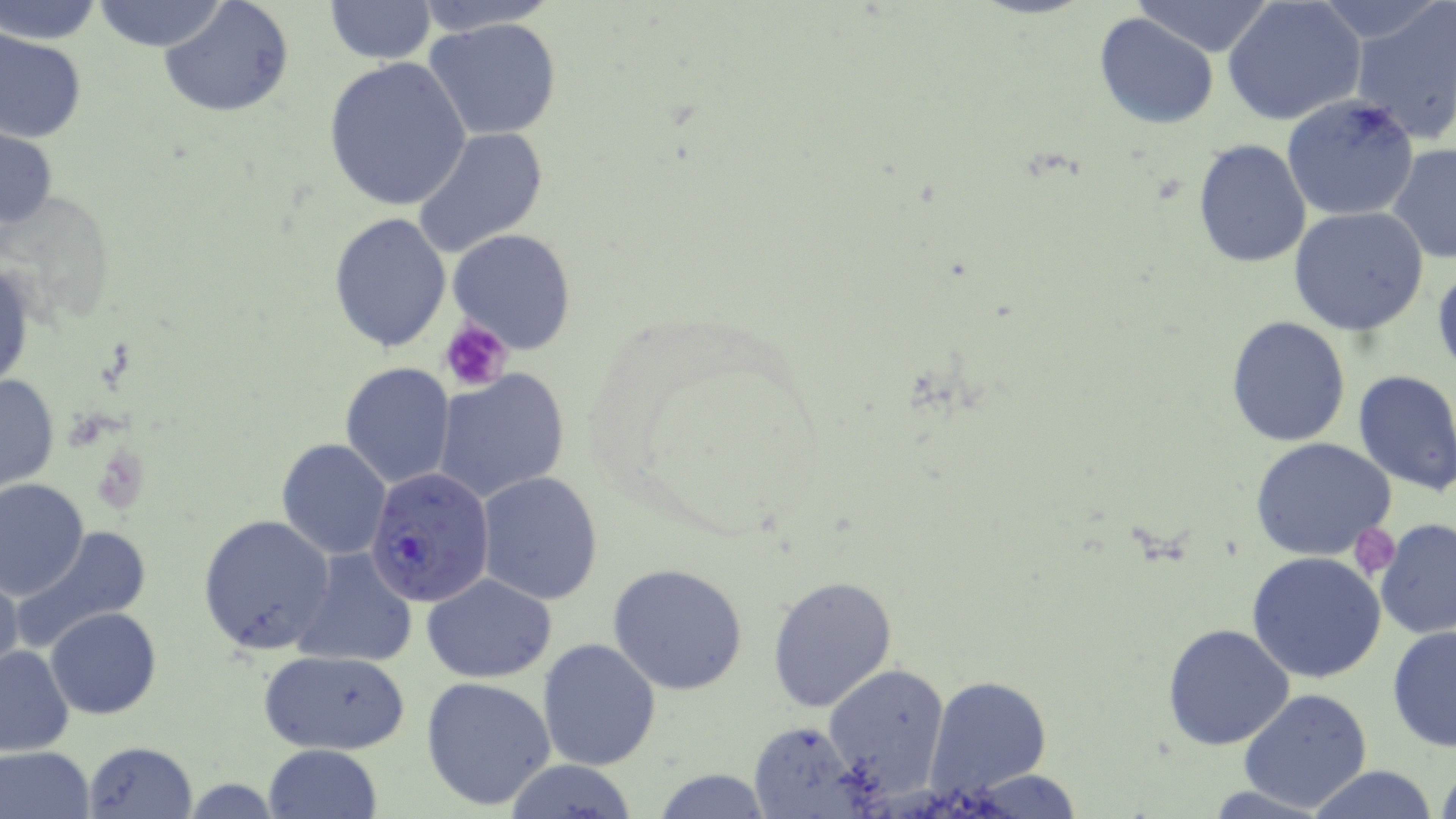

Summary:
  - Coordinate format: approximate bounding boxes as named x1/y1/x2/y2 corners in pixels
  - Uninfected red blood cell locations: (x1=91, y1=0, x2=229, y2=53), (x1=321, y1=0, x2=436, y2=64), (x1=411, y1=0, x2=560, y2=35), (x1=1223, y1=0, x2=1367, y2=126), (x1=2, y1=1, x2=104, y2=45), (x1=158, y1=1, x2=295, y2=117), (x1=1131, y1=1, x2=1277, y2=57), (x1=1350, y1=1, x2=1456, y2=146), (x1=1093, y1=12, x2=1219, y2=130), (x1=425, y1=17, x2=562, y2=141), (x1=0, y1=29, x2=86, y2=144), (x1=322, y1=56, x2=472, y2=211), (x1=1281, y1=94, x2=1422, y2=223), (x1=0, y1=125, x2=57, y2=236), (x1=411, y1=127, x2=549, y2=258), (x1=1191, y1=138, x2=1311, y2=269), (x1=1386, y1=143, x2=1456, y2=267), (x1=1287, y1=206, x2=1429, y2=336), (x1=329, y1=211, x2=453, y2=353), (x1=448, y1=228, x2=578, y2=354), (x1=1, y1=259, x2=34, y2=396), (x1=1431, y1=263, x2=1456, y2=379), (x1=1225, y1=316, x2=1350, y2=448), (x1=340, y1=362, x2=455, y2=489), (x1=1352, y1=368, x2=1456, y2=493), (x1=431, y1=369, x2=570, y2=502), (x1=0, y1=372, x2=59, y2=493), (x1=1249, y1=437, x2=1396, y2=560), (x1=276, y1=438, x2=392, y2=558), (x1=475, y1=472, x2=604, y2=607), (x1=0, y1=479, x2=89, y2=599), (x1=198, y1=514, x2=335, y2=654), (x1=1373, y1=518, x2=1456, y2=640), (x1=10, y1=525, x2=154, y2=652), (x1=292, y1=548, x2=418, y2=666), (x1=1246, y1=551, x2=1389, y2=684), (x1=608, y1=563, x2=748, y2=695), (x1=0, y1=566, x2=22, y2=685), (x1=422, y1=572, x2=556, y2=682), (x1=767, y1=572, x2=898, y2=713), (x1=46, y1=607, x2=161, y2=719), (x1=1162, y1=624, x2=1295, y2=749), (x1=1387, y1=624, x2=1456, y2=752), (x1=538, y1=637, x2=661, y2=770), (x1=0, y1=643, x2=76, y2=755), (x1=259, y1=648, x2=411, y2=755), (x1=823, y1=664, x2=951, y2=795), (x1=420, y1=675, x2=557, y2=810), (x1=925, y1=676, x2=1053, y2=798), (x1=1237, y1=689, x2=1372, y2=813), (x1=746, y1=721, x2=868, y2=818), (x1=84, y1=741, x2=196, y2=817), (x1=263, y1=744, x2=382, y2=819), (x1=0, y1=746, x2=97, y2=819), (x1=1433, y1=756, x2=1456, y2=819), (x1=499, y1=759, x2=642, y2=818), (x1=1304, y1=765, x2=1438, y2=819), (x1=648, y1=766, x2=774, y2=819), (x1=958, y1=770, x2=1088, y2=817)
  - Plasmodium falciparum-infected red blood cell locations: (x1=365, y1=467, x2=495, y2=606)
  - Platelet locations: (x1=439, y1=320, x2=515, y2=393), (x1=1353, y1=529, x2=1401, y2=576)
  - Slide-level diagnosis: Plasmodium falciparum
  - Modality: light microscopy
  - Stain: May-Grünwald-Giemsa
  - Magnification: 1000x
  - Image size: 1456×819 pixels
  - Field of view: one of a larger specimen
  - Preparation: thin blood smear